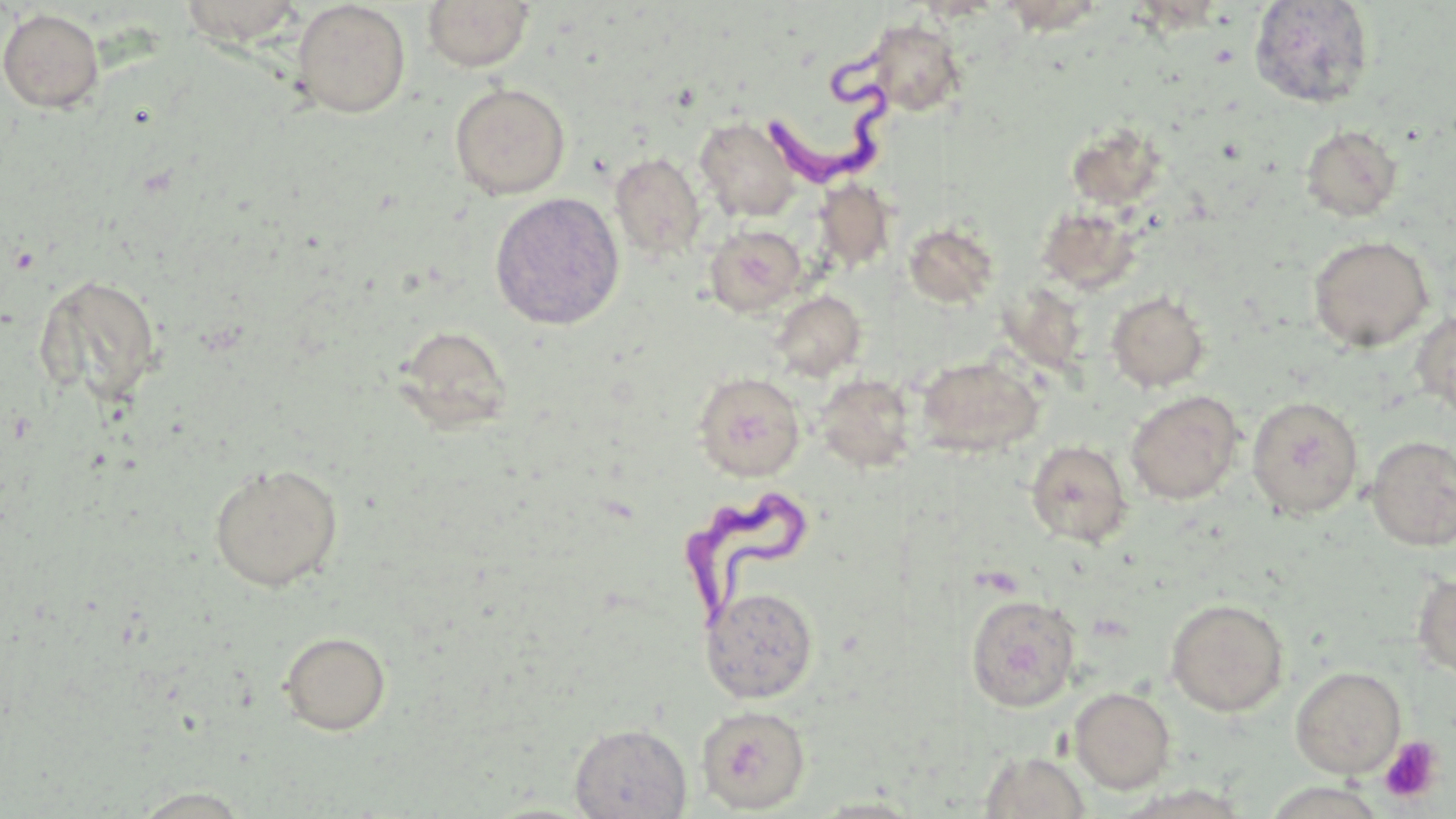 Approximate bounding boxes as [x1, y1, x2, y2] in pixels. Platelet locations: [1378, 736, 1444, 805]. Trypanosoma brucei locations: [764, 41, 896, 198], [678, 489, 804, 633]. Uninfected red blood cell locations: [1249, 0, 1376, 109], [176, 1, 309, 47], [292, 1, 411, 118], [421, 1, 535, 71], [0, 8, 105, 113], [864, 19, 966, 117], [450, 82, 570, 200], [695, 117, 801, 222], [1066, 122, 1166, 211], [1300, 125, 1403, 222], [610, 152, 706, 261], [813, 179, 896, 272], [490, 192, 625, 330], [1037, 205, 1142, 294], [904, 222, 999, 308], [704, 225, 806, 316], [1308, 235, 1434, 352], [34, 273, 163, 407], [770, 291, 866, 381], [1106, 291, 1211, 392], [1410, 309, 1456, 422], [394, 324, 512, 434], [916, 356, 1044, 457], [693, 371, 806, 481], [815, 374, 917, 472], [1125, 390, 1244, 505], [1247, 396, 1364, 520], [1366, 435, 1456, 550], [1026, 440, 1133, 547], [208, 462, 344, 592], [1412, 571, 1456, 681], [701, 585, 819, 703], [965, 593, 1081, 712], [1165, 598, 1288, 717], [279, 631, 391, 736], [1290, 665, 1407, 779], [1069, 687, 1176, 794], [696, 705, 810, 814], [569, 722, 692, 818], [977, 751, 1093, 819], [129, 787, 258, 817], [807, 797, 928, 818]. Slide-level diagnosis: Trypanosoma brucei. Optical microscopy. One field of a larger specimen. Image is 1456×819 pixels. Thin blood film. May-Grünwald-Giemsa stain. Captured at 1000x magnification.